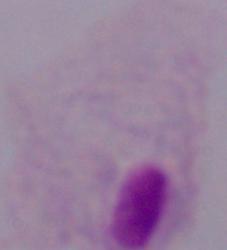
Summary:
  - Magnification: 1000x
  - Identification: trichomonad
  - Modality: photomicrograph